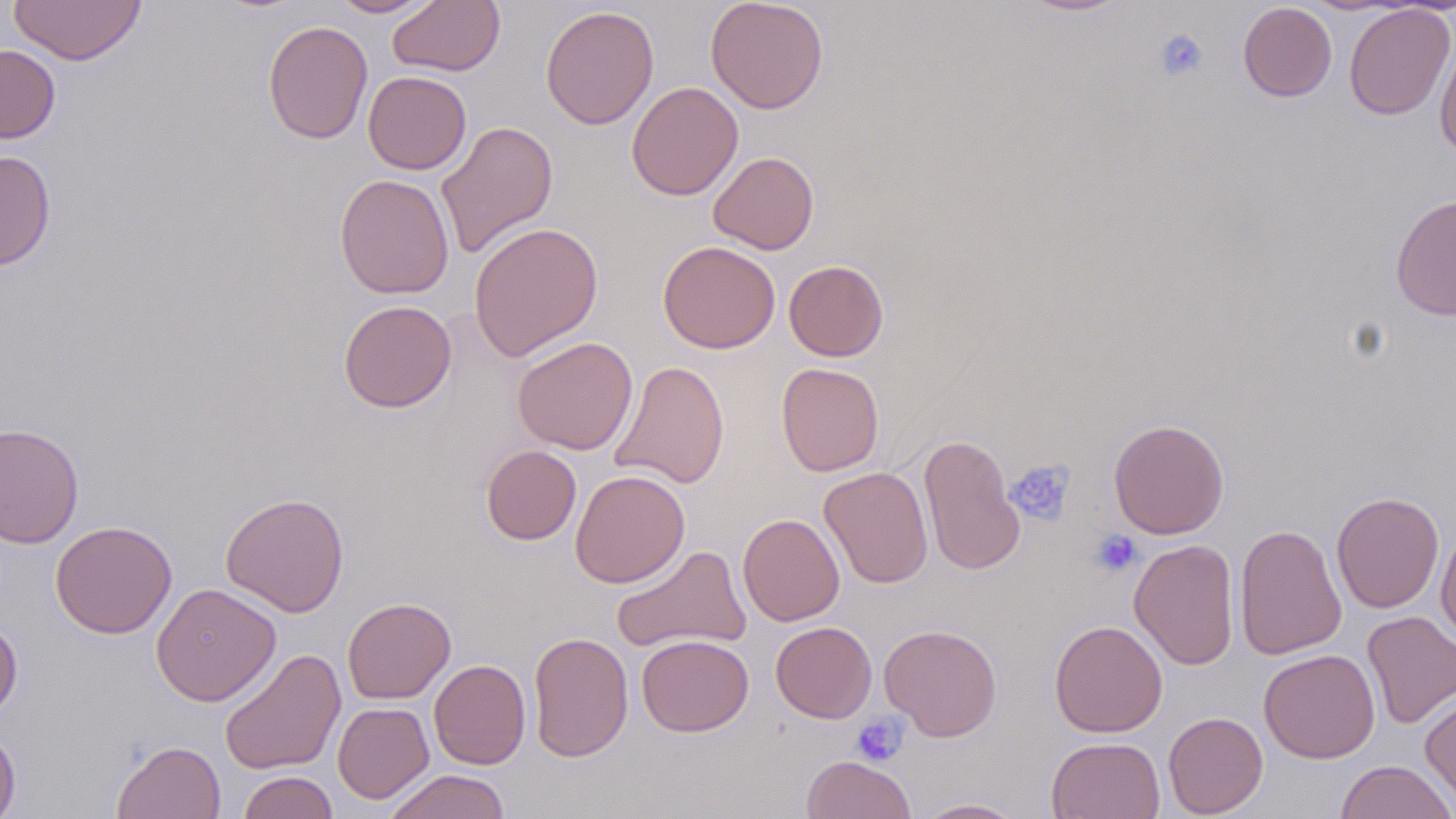

Approximate bounding boxes as (x1,y1)-(x2,y2) corner pairs in pixels. Platelet locations: (1154,29)-(1209,83), (1005,460)-(1075,525), (1090,529)-(1144,578), (850,714)-(909,766). Uninfected red blood cell locations: (8,0)-(146,66), (329,0)-(442,18), (387,0)-(505,77), (705,0)-(829,113), (1019,0)-(1133,16), (1238,2)-(1337,102), (1343,4)-(1455,120), (540,5)-(659,130), (262,20)-(374,144), (1434,36)-(1456,159), (0,44)-(60,143), (363,71)-(472,174), (626,81)-(743,201), (436,120)-(559,259), (0,151)-(56,270), (708,151)-(819,254), (334,174)-(455,299), (1390,194)-(1456,320), (468,221)-(603,362), (658,241)-(780,354), (784,260)-(888,361), (338,300)-(457,412), (512,336)-(638,455), (610,360)-(730,488), (776,362)-(884,476), (1108,419)-(1230,539), (0,422)-(84,549), (919,433)-(1025,575), (481,445)-(582,545), (819,467)-(933,589), (570,469)-(690,588), (1331,491)-(1444,613), (220,492)-(349,617), (738,513)-(845,626), (50,520)-(177,639), (1436,522)-(1456,647), (1234,523)-(1347,660), (1129,539)-(1240,670), (612,544)-(751,654), (151,583)-(281,706), (342,597)-(456,704), (1362,611)-(1456,729), (0,616)-(22,721), (1049,620)-(1168,737), (770,621)-(877,723), (879,624)-(1002,741), (528,631)-(633,761), (636,634)-(754,736), (219,649)-(346,775), (1259,649)-(1380,763), (429,659)-(531,769), (1420,692)-(1456,811), (333,702)-(433,803), (1163,711)-(1268,817), (0,726)-(21,819), (1046,737)-(1165,819), (112,740)-(226,819), (802,755)-(917,819), (1334,759)-(1455,819), (383,769)-(511,819), (238,770)-(338,819), (912,798)-(1028,818). Slide-level diagnosis: no evidence of blood parasites. Thin blood smear. May-Grünwald-Giemsa stain. 1000x magnification. Single field of view. Light microscopy. Image is 1456×819 pixels.